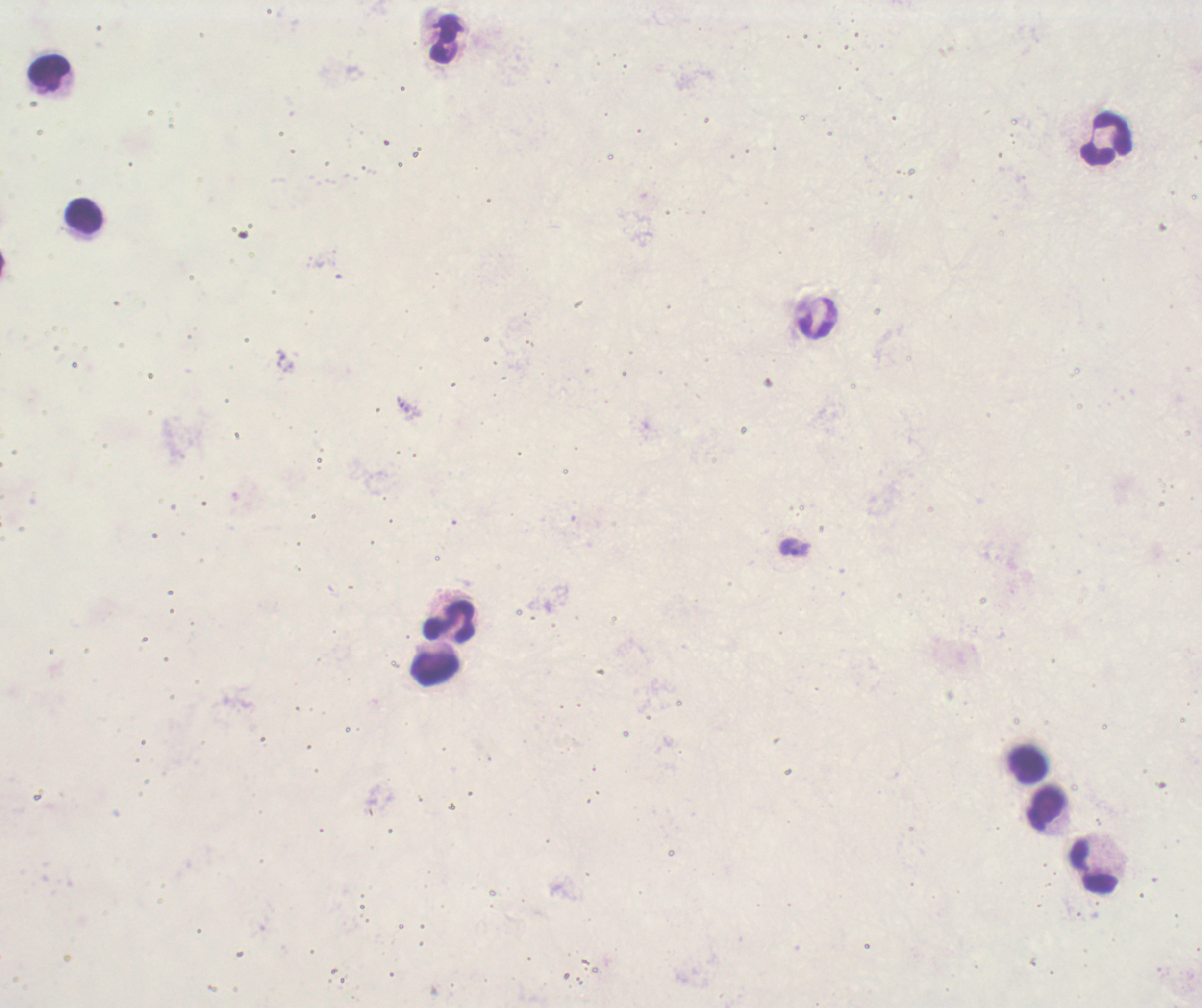
Approximate centers as {x, y} in pixels.
Summary:
  - Leukocyte locations: {444, 40}, {48, 72}, {1106, 139}, {85, 215}, {450, 621}, {435, 670}, {1027, 765}, {1046, 809}, {1094, 865}
  - Trophozoite locations: {794, 547}
  - Context: previously used in an actual diagnosis
  - Background quality: unsatisfactory
  - Image size: 1202×1008 pixels
  - Field of view: single
  - Preparation: thick smear of blood
  - Coloration quality: bad
  - Result: Plasmodium parasites detected
  - Magnification: 100x
  - Stain: Romanowsky